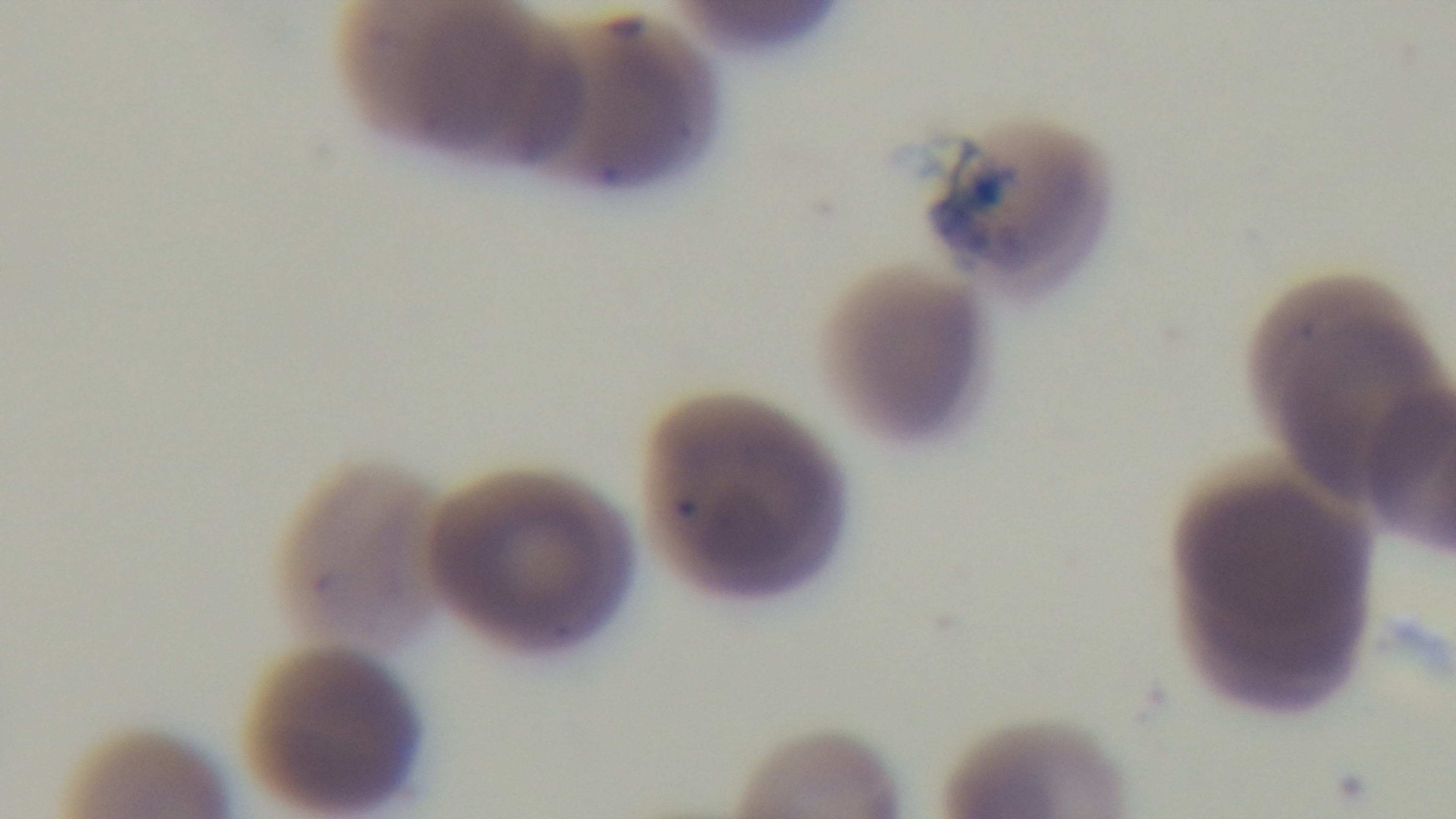

Summary:
  - Modality: light microscopy
  - Field of view: single
  - Objective: 100x oil immersion
  - Preparation: thin blood film
  - Malaria status: positive
  - Stain: Giemsa
  - Capture: mounted 4K digital camera